Report the malaria status of this cell.
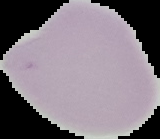

Uninfected.

From a thin blood film. Image is 160×139 pixels. Cell region segmented out of the field of view; the surrounding area is masked to black.